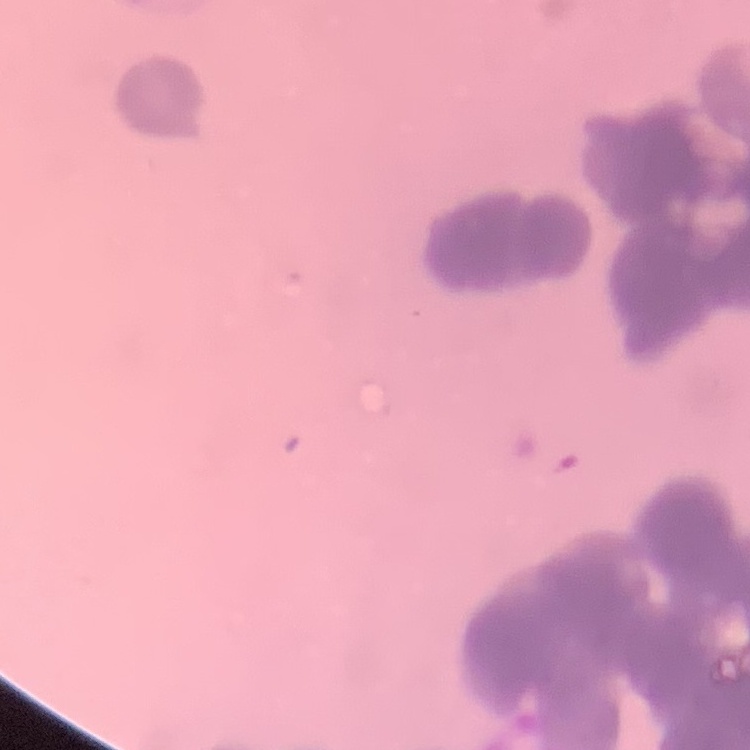

The erythrocytes exhibit rouleaux formation. Thin blood smear. Field's or Giemsa stain. Square crop of a larger photomicrograph.